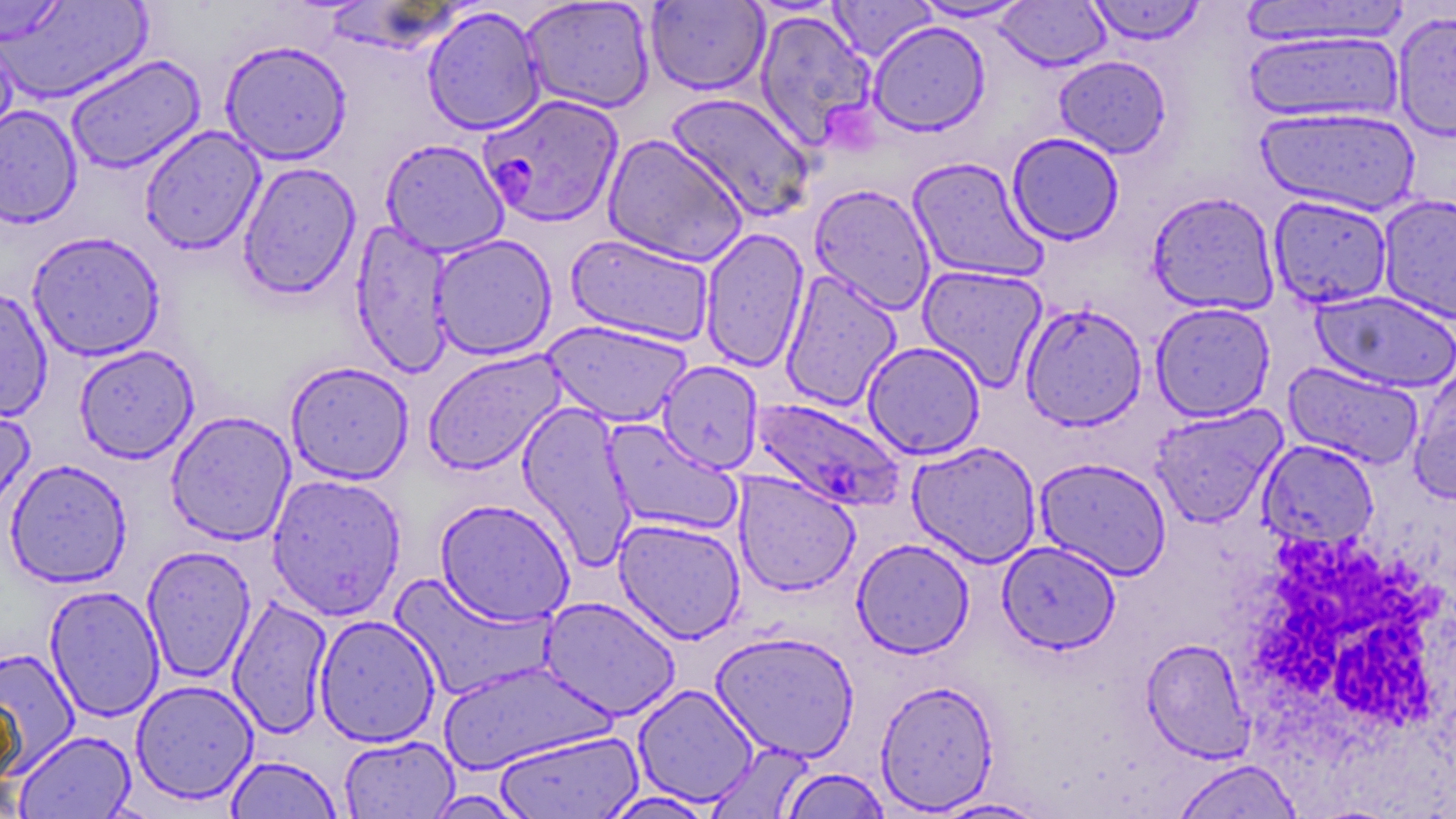
Summary:
  - Coordinate format: approximate bounding boxes as (x1,y1)-(x2,y2) corner pairs in pixels
  - White blood cell locations: (1230,529)-(1455,797)
  - Plasmodium falciparum-infected red blood cell locations: (478,93)-(624,228), (750,397)-(907,513)
  - Uninfected red blood cell locations: (0,0)-(153,105), (519,0)-(656,114), (828,0)-(936,63), (910,0)-(1034,22), (1086,0)-(1205,45), (1238,0)-(1413,49), (1,1)-(68,44), (645,1)-(770,95), (995,1)-(1111,71), (422,6)-(545,135), (753,9)-(878,153), (1391,10)-(1456,142), (867,21)-(991,137), (1243,29)-(1404,126), (0,32)-(19,157), (219,40)-(352,165), (65,54)-(205,175), (1053,55)-(1172,159), (666,92)-(817,222), (0,104)-(83,229), (1254,105)-(1421,217), (139,125)-(265,255), (1007,132)-(1125,246), (602,134)-(749,267), (380,138)-(510,258), (907,156)-(1048,284), (237,161)-(362,300), (809,184)-(936,315), (1146,191)-(1280,315), (1377,194)-(1456,324), (1268,195)-(1393,309), (350,219)-(455,378), (699,227)-(810,373), (26,230)-(166,361), (565,233)-(716,347), (429,234)-(557,360), (917,263)-(1050,391), (780,269)-(903,412), (0,287)-(54,422), (1311,290)-(1456,393), (1019,302)-(1148,431), (1150,302)-(1276,422), (542,319)-(693,427), (862,341)-(986,459), (74,344)-(199,464), (422,350)-(566,476), (285,360)-(414,484), (657,361)-(764,473), (1283,361)-(1425,470), (1408,364)-(1456,505), (0,393)-(35,523), (516,402)-(637,568), (1148,404)-(1287,528), (165,411)-(296,546), (602,419)-(743,537), (1258,439)-(1379,549), (907,440)-(1042,568), (1034,456)-(1172,580), (4,459)-(132,587), (732,471)-(860,596), (266,473)-(407,620), (434,497)-(576,626), (613,517)-(746,643), (852,538)-(975,658), (997,540)-(1121,654), (141,545)-(256,683), (389,572)-(554,701), (44,585)-(165,721), (227,595)-(333,739), (538,596)-(681,720), (314,614)-(441,747), (710,630)-(860,763), (1140,638)-(1255,762), (0,647)-(80,775), (437,660)-(615,775), (131,679)-(259,804), (875,679)-(999,814), (632,684)-(759,807), (0,691)-(24,794), (493,729)-(643,818), (15,730)-(137,818), (338,734)-(459,818), (705,741)-(816,819), (225,755)-(342,818), (1171,759)-(1304,819), (779,767)-(891,818), (422,790)-(534,818), (599,790)-(719,818), (929,796)-(1052,817)
  - Slide-level diagnosis: Plasmodium falciparum
  - Image size: 1456×819 pixels
  - Stain: May-Grünwald-Giemsa
  - Field of view: single
  - Modality: optical microscopy
  - Preparation: thin blood film
  - Magnification: 1000x